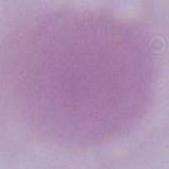
magnification = 1000x
identification = erythrocyte
modality = photomicrograph